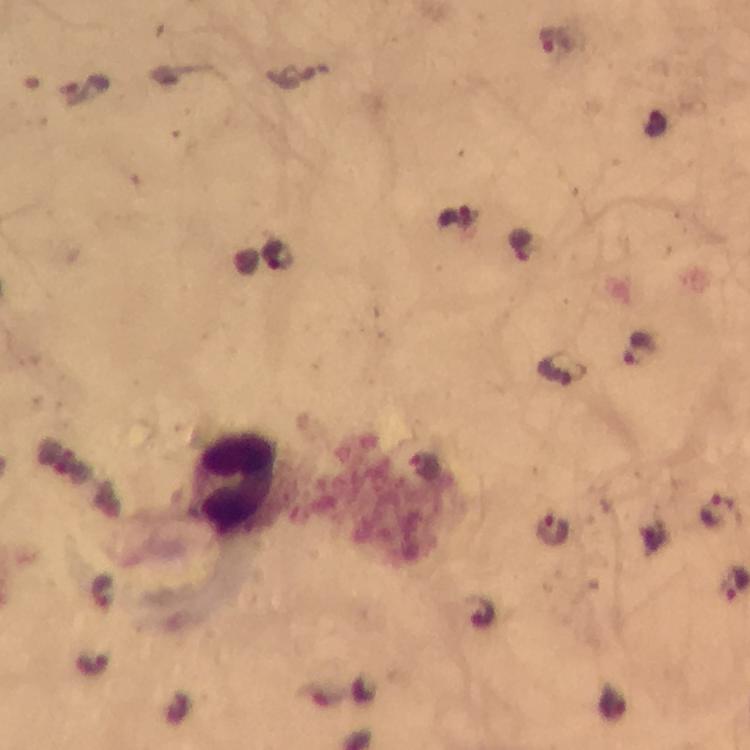
magnification = 100x
image size = 750×750 pixels
immersion oil = used
preparation = thick blood smear
capture = smartphone mounted on the microscope
Plasmodium parasite locations = approximate centers as (x, y) in pixels: (558, 39), (454, 219), (521, 244), (276, 254), (640, 347), (561, 369), (425, 465), (720, 511), (553, 528), (104, 591)
leukocyte locations = approximate centers as (x, y) in pixels: (235, 479)
cropped from = one field of view
stain = Giemsa
context = from a diagnostic examination for malaria